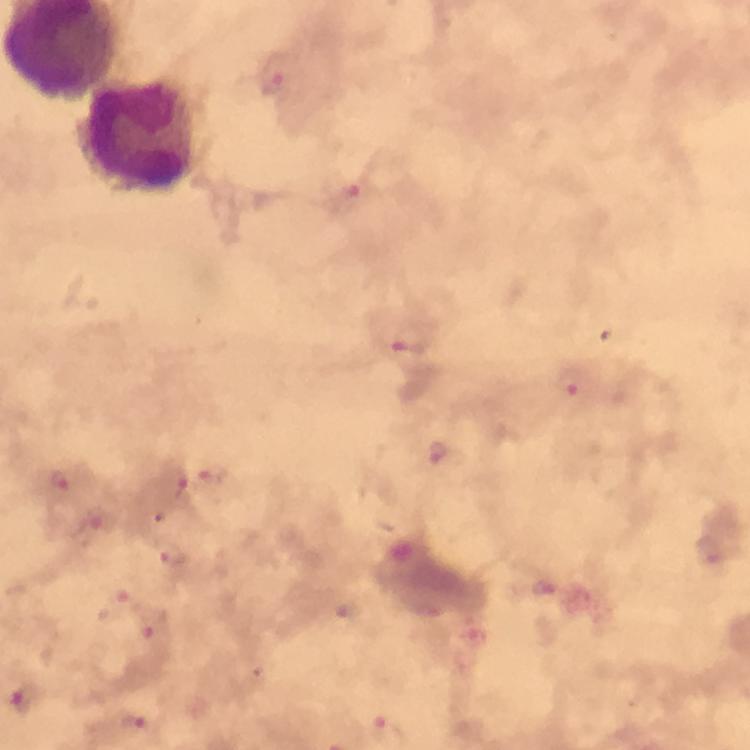

context = from a malaria diagnostic workup
image size = 750×750 pixels
Plasmodium parasite locations = approximate centers as {x, y} in pixels: {273, 75}, {354, 199}, {411, 339}, {572, 384}, {442, 455}, {212, 476}, {60, 480}, {176, 485}, {96, 518}, {710, 550}, {173, 555}, {545, 588}, {153, 624}, {27, 698}, {131, 722}
immersion oil = applied
leukocyte locations = approximate centers as {x, y} in pixels: {138, 136}
preparation = thick blood film
cropped from = a single field of view
magnification = 100x
stain = Giemsa
capture = smartphone photograph through a microscope